Locate and identify every blood parasite.
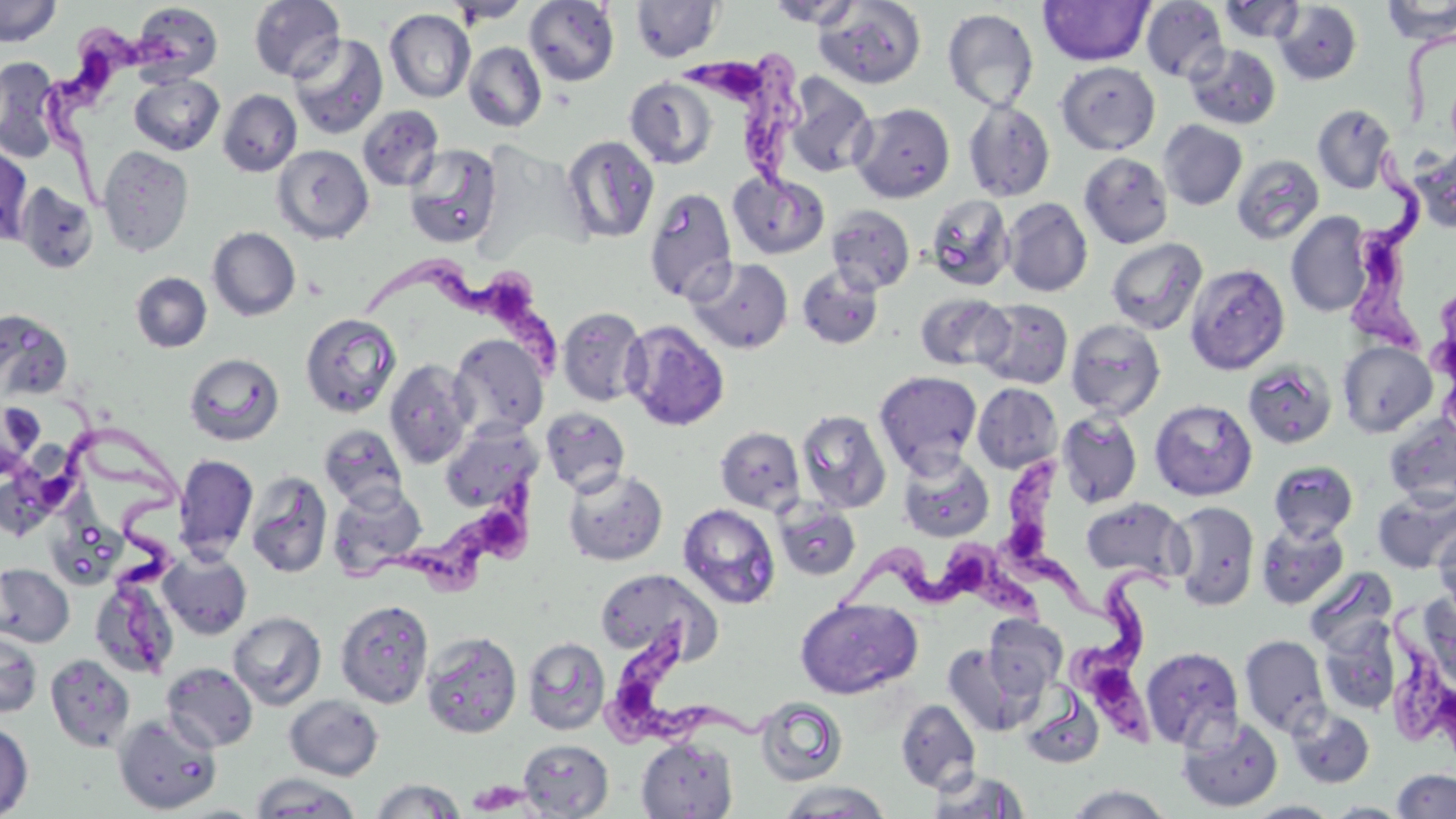
Approximate bounding boxes as (x1, y1, x2, y2) in pixels.
Trypanosoma brucei: (29, 15, 193, 207), (693, 53, 808, 220), (1334, 148, 1426, 365), (365, 261, 570, 377), (60, 389, 181, 670), (3, 409, 198, 523), (999, 456, 1113, 620), (363, 458, 548, 597), (839, 542, 1054, 643), (1068, 558, 1192, 757), (1374, 601, 1456, 754), (593, 616, 778, 749).
No Plasmodium falciparum, Plasmodium ovale, Plasmodium malariae, Plasmodium vivax, or Babesia divergens observed.

Uninfected red blood cell locations: (0, 0, 62, 47), (248, 0, 345, 82), (447, 0, 531, 25), (524, 0, 619, 87), (630, 0, 724, 62), (1140, 0, 1229, 83), (1381, 0, 1456, 43), (764, 1, 865, 28), (1038, 1, 1154, 66), (1218, 1, 1306, 44), (814, 2, 926, 88), (1273, 2, 1363, 85), (131, 3, 222, 84), (942, 8, 1039, 111), (384, 9, 475, 103), (289, 33, 388, 139), (463, 42, 547, 132), (1185, 44, 1281, 129), (0, 56, 63, 162), (1056, 61, 1160, 155), (129, 72, 224, 155), (783, 74, 876, 179), (625, 77, 717, 168), (218, 89, 302, 177), (962, 98, 1055, 202), (850, 102, 955, 203), (1313, 104, 1396, 194), (357, 105, 444, 191), (1158, 120, 1247, 210), (561, 135, 659, 244), (403, 143, 503, 249), (0, 145, 33, 246), (272, 145, 374, 244), (1412, 145, 1456, 234), (97, 146, 194, 257), (1079, 152, 1173, 249), (1231, 155, 1325, 245), (728, 171, 829, 260), (14, 183, 99, 274), (643, 187, 738, 304), (925, 193, 1015, 291), (1002, 198, 1093, 297), (826, 205, 915, 295), (1286, 211, 1375, 317), (208, 227, 301, 321), (1106, 237, 1207, 335), (686, 257, 793, 354), (1185, 263, 1290, 375), (797, 265, 884, 349), (130, 272, 212, 353), (916, 294, 1012, 371), (975, 298, 1073, 389), (557, 307, 649, 407), (0, 310, 73, 402), (300, 313, 401, 417), (1065, 318, 1166, 420), (622, 319, 730, 432), (449, 334, 549, 438), (1338, 341, 1438, 438), (184, 352, 284, 446), (384, 359, 476, 469), (1242, 360, 1338, 449), (874, 371, 983, 473), (972, 382, 1063, 473), (1150, 399, 1257, 501), (0, 400, 45, 477), (541, 408, 631, 496), (797, 409, 891, 513), (1056, 410, 1142, 508), (1384, 416, 1456, 508), (440, 423, 538, 513), (318, 424, 408, 510), (715, 427, 805, 515), (897, 450, 994, 543), (173, 454, 258, 562), (1269, 460, 1358, 541), (562, 467, 668, 566), (244, 471, 333, 579), (327, 483, 427, 579), (1373, 489, 1456, 573), (1081, 496, 1191, 583), (774, 500, 861, 581), (1168, 501, 1260, 611), (678, 504, 781, 609), (47, 512, 127, 589), (1256, 520, 1349, 609), (1435, 522, 1456, 620), (158, 551, 252, 639), (0, 563, 75, 647), (1304, 566, 1398, 656), (594, 568, 721, 663), (90, 574, 180, 680), (1416, 590, 1456, 693), (795, 598, 923, 699), (335, 599, 435, 709), (228, 611, 326, 710), (982, 615, 1067, 700), (1318, 619, 1402, 715), (0, 628, 43, 718), (420, 631, 522, 739), (1239, 633, 1331, 738), (522, 637, 611, 735), (943, 644, 1036, 736), (1140, 646, 1244, 751), (45, 653, 137, 753), (161, 662, 258, 752), (1020, 688, 1105, 769), (284, 695, 384, 781), (755, 697, 848, 786), (896, 699, 981, 793), (1288, 705, 1375, 788), (112, 713, 222, 813), (1176, 717, 1283, 812), (0, 720, 34, 818), (636, 737, 739, 818), (518, 739, 614, 818), (926, 768, 1030, 818), (1392, 768, 1456, 818), (251, 773, 362, 818), (369, 778, 467, 818), (775, 781, 893, 818), (1063, 785, 1173, 819), (1243, 801, 1342, 818), (1323, 801, 1413, 818). Slide-level diagnosis: Trypanosoma brucei. May-Grünwald-Giemsa-stained preparation. Image is 1456×819 pixels. Optical microscopy. Thin blood smear. Single field of view. Captured at 1000x magnification.